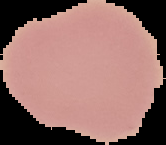

Summary:
  - Preparation: thin blood smear
  - Result: no Plasmodium parasites seen
  - Image size: 166×145 pixels
  - Image type: cell region segmented out of the field of view; surrounding area masked to black